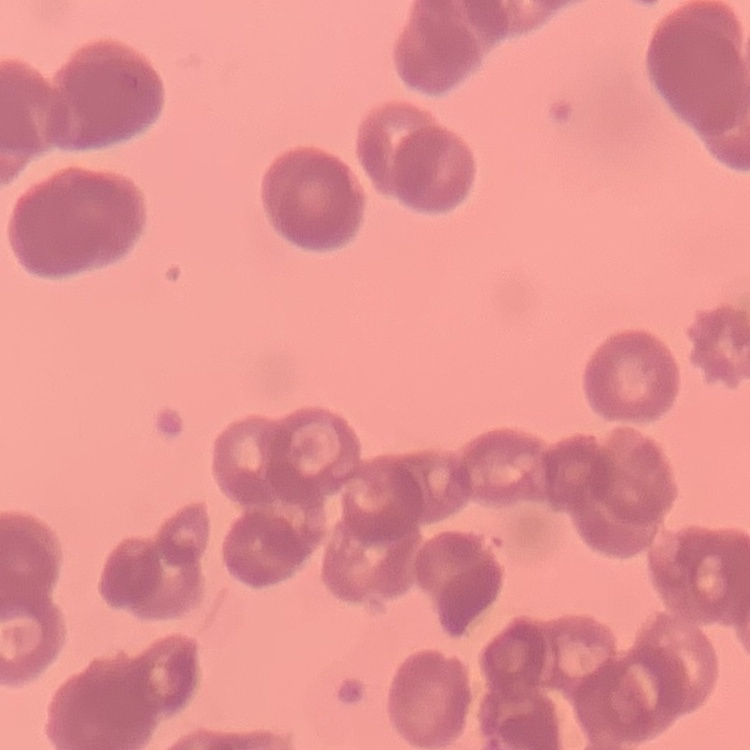
The red blood cells show rouleaux formation. Thin blood film. Square crop of a larger photomicrograph. Stained with either Field's or Giemsa.